Give the position of every Plasmodium parasite visible.
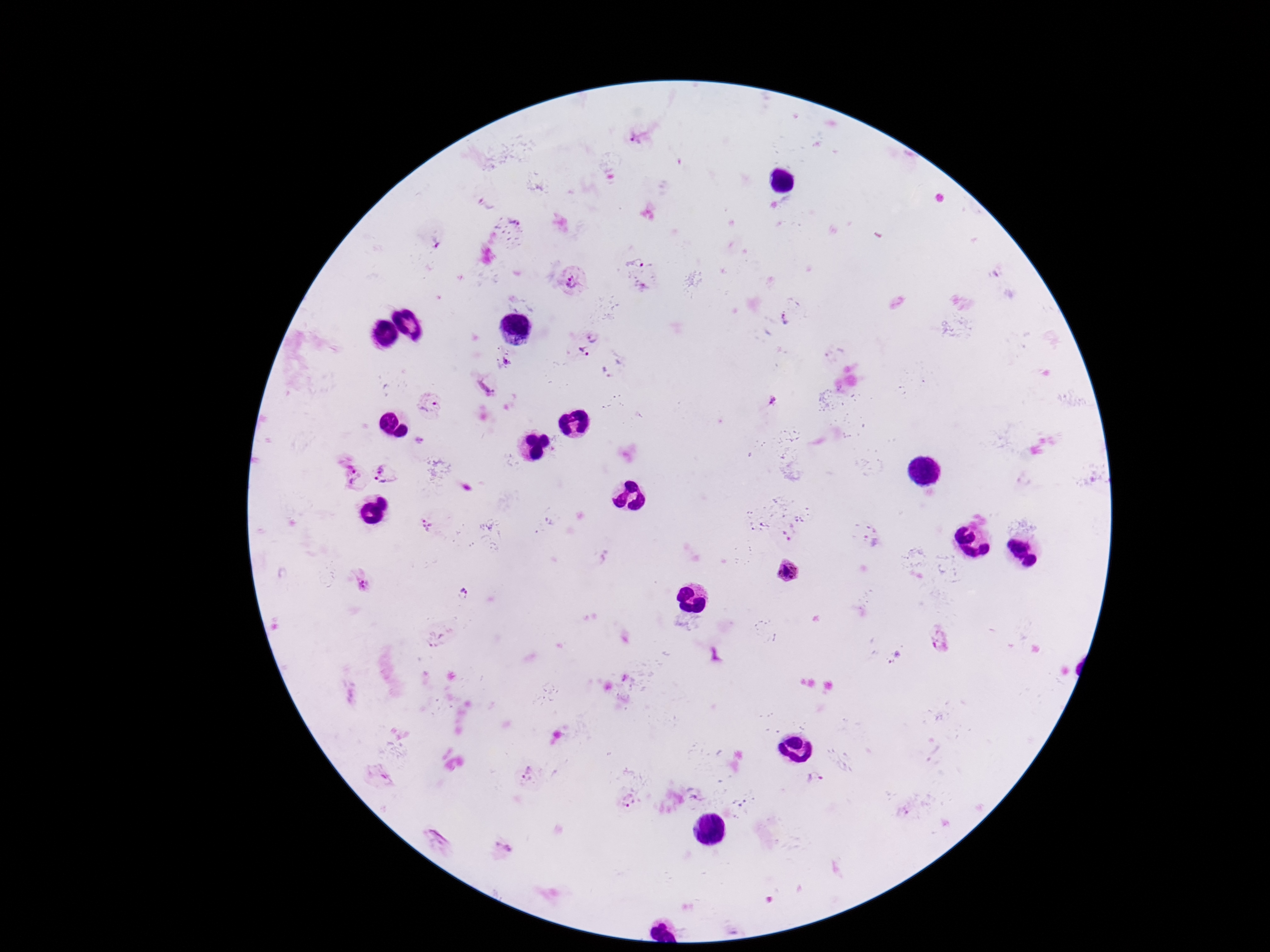

Approximate centers as {x, y} in pixels.
Plasmodium parasites: {639, 137}, {512, 226}, {637, 260}, {575, 281}, {786, 319}, {591, 336}, {582, 353}, {507, 361}, {607, 373}, {486, 384}, {773, 404}, {430, 405}, {350, 473}, {385, 473}, {427, 525}, {785, 572}, {361, 581}, {463, 593}, {437, 641}, {940, 641}, {896, 659}, {624, 678}, {528, 773}, {380, 777}, {816, 781}, {627, 800}, {440, 840}, {503, 848}.

Giemsa-stained preparation. One field from this slide. Thick blood smear. Image is 1270×952 pixels. Patient malaria status: positive. 100x magnification. Smartphone photograph taken through the microscope eyepiece.